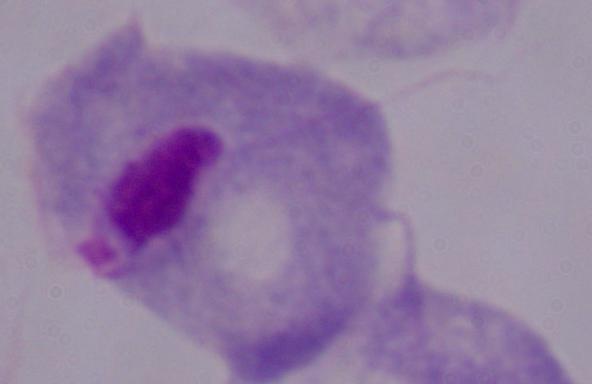 A trichomonad is seen. Micrograph. 1000x magnification.